Identify the preparation type.
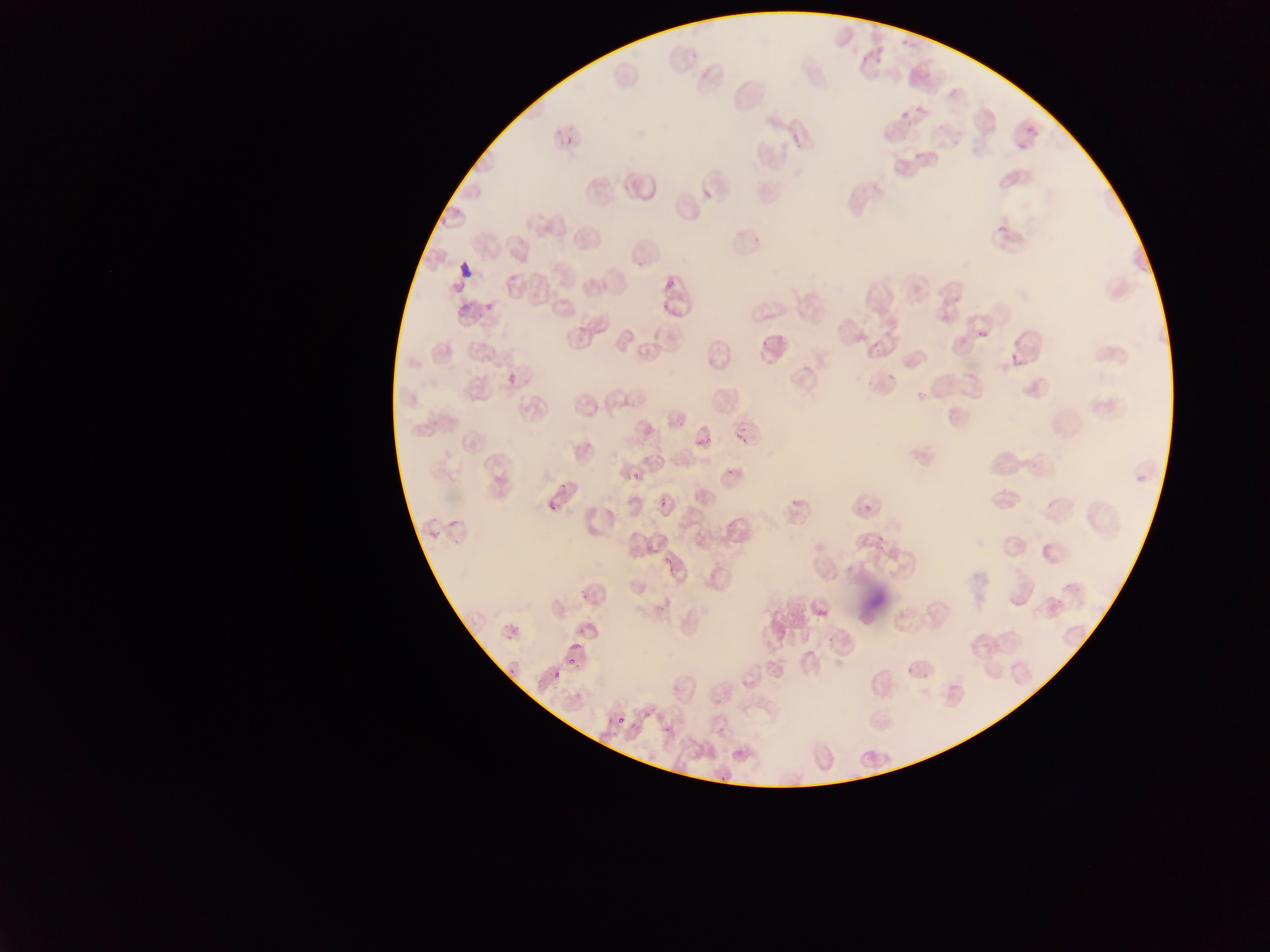

Thin blood film.

image size = 1270×952 pixels
capture = mobile-phone photograph through a microscope
country = Ghana
field of view = single
leukocyte locations = approximate bounding boxes as (left, top, right, bottom) in pixels: (755, 326, 795, 371)
Plasmodium parasite locations = approximate bounding boxes as (left, top, right, bottom) in pixels: (898, 106, 916, 120), (1022, 118, 1035, 132), (563, 136, 577, 144), (1015, 142, 1028, 150), (972, 325, 992, 348), (733, 423, 752, 449), (690, 425, 712, 455), (629, 467, 646, 484), (558, 477, 572, 491), (656, 495, 671, 512), (546, 500, 558, 517), (860, 503, 873, 513), (664, 554, 675, 571), (579, 593, 591, 609), (813, 607, 832, 619), (571, 638, 585, 655), (563, 651, 582, 668), (905, 660, 915, 674), (508, 661, 521, 683), (551, 672, 561, 684), (641, 705, 653, 724), (614, 711, 628, 729), (659, 725, 673, 735), (715, 768, 725, 782)